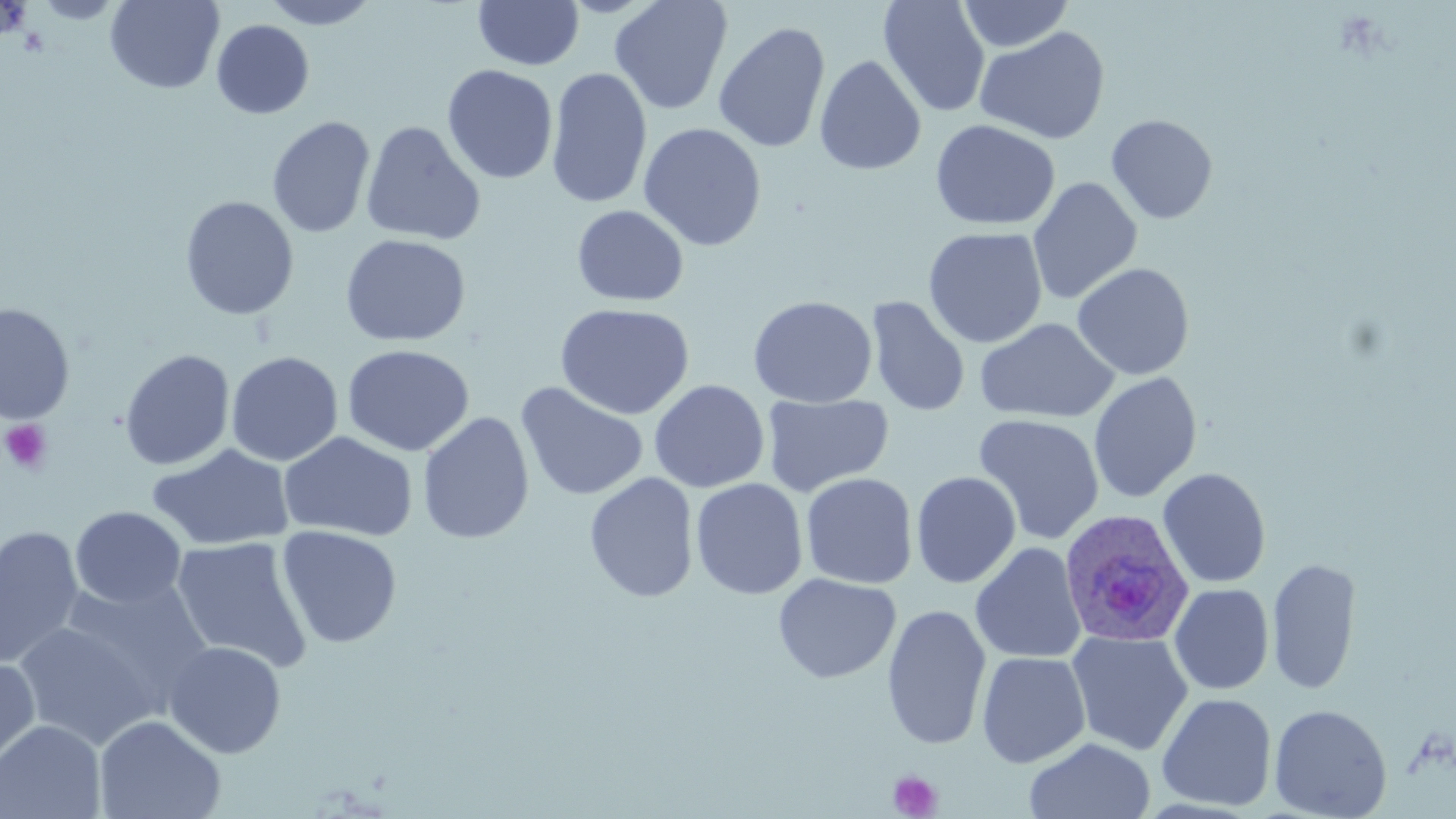

Approximate bounding boxes as named x1/y1/x2/y2 corners in pixels. Platelet locations: (x1=1, y1=419, x2=53, y2=474), (x1=888, y1=770, x2=942, y2=818). Uninfected red blood cell locations: (x1=106, y1=0, x2=224, y2=94), (x1=260, y1=0, x2=382, y2=30), (x1=609, y1=0, x2=733, y2=115), (x1=878, y1=0, x2=991, y2=117), (x1=957, y1=0, x2=1074, y2=52), (x1=473, y1=1, x2=584, y2=70), (x1=211, y1=19, x2=314, y2=119), (x1=713, y1=21, x2=832, y2=154), (x1=975, y1=26, x2=1111, y2=145), (x1=814, y1=54, x2=927, y2=176), (x1=442, y1=64, x2=558, y2=184), (x1=545, y1=67, x2=653, y2=210), (x1=1106, y1=113, x2=1218, y2=224), (x1=267, y1=116, x2=377, y2=238), (x1=930, y1=119, x2=1061, y2=231), (x1=360, y1=121, x2=486, y2=246), (x1=639, y1=122, x2=766, y2=251), (x1=1028, y1=176, x2=1143, y2=306), (x1=180, y1=195, x2=300, y2=320), (x1=571, y1=205, x2=689, y2=307), (x1=923, y1=227, x2=1048, y2=348), (x1=339, y1=233, x2=471, y2=346), (x1=1072, y1=262, x2=1195, y2=381), (x1=747, y1=295, x2=878, y2=408), (x1=866, y1=296, x2=970, y2=417), (x1=1, y1=302, x2=75, y2=425), (x1=554, y1=302, x2=695, y2=419), (x1=975, y1=317, x2=1120, y2=423), (x1=342, y1=344, x2=475, y2=457), (x1=119, y1=349, x2=235, y2=471), (x1=225, y1=351, x2=344, y2=466), (x1=1088, y1=372, x2=1202, y2=504), (x1=649, y1=379, x2=769, y2=493), (x1=515, y1=381, x2=650, y2=502), (x1=761, y1=393, x2=893, y2=497), (x1=417, y1=412, x2=535, y2=544), (x1=972, y1=414, x2=1105, y2=545), (x1=278, y1=431, x2=417, y2=542), (x1=147, y1=443, x2=295, y2=551), (x1=1157, y1=468, x2=1271, y2=588), (x1=911, y1=471, x2=1022, y2=589), (x1=584, y1=472, x2=699, y2=603), (x1=801, y1=473, x2=918, y2=589), (x1=690, y1=478, x2=808, y2=600), (x1=70, y1=506, x2=187, y2=609), (x1=0, y1=524, x2=84, y2=670), (x1=276, y1=525, x2=403, y2=648), (x1=170, y1=535, x2=314, y2=674), (x1=970, y1=542, x2=1088, y2=664), (x1=1267, y1=556, x2=1361, y2=695), (x1=773, y1=573, x2=901, y2=684), (x1=60, y1=576, x2=215, y2=712), (x1=1169, y1=583, x2=1274, y2=695), (x1=882, y1=603, x2=992, y2=750), (x1=12, y1=621, x2=159, y2=751), (x1=1067, y1=630, x2=1193, y2=756), (x1=163, y1=641, x2=286, y2=759), (x1=976, y1=651, x2=1091, y2=769), (x1=0, y1=656, x2=41, y2=775), (x1=1156, y1=692, x2=1277, y2=812), (x1=1268, y1=703, x2=1393, y2=819), (x1=94, y1=714, x2=226, y2=819), (x1=0, y1=720, x2=106, y2=819), (x1=1024, y1=736, x2=1156, y2=819). Plasmodium ovale-infected red blood cell locations: (x1=1058, y1=509, x2=1195, y2=648). Slide-level diagnosis: Plasmodium ovale. Thin blood smear. Captured at 1000x magnification. May-Grünwald-Giemsa stain. One field of a larger specimen. Image is 1456×819 pixels. Optical microscopy.